Assess for Plasmodium parasites.
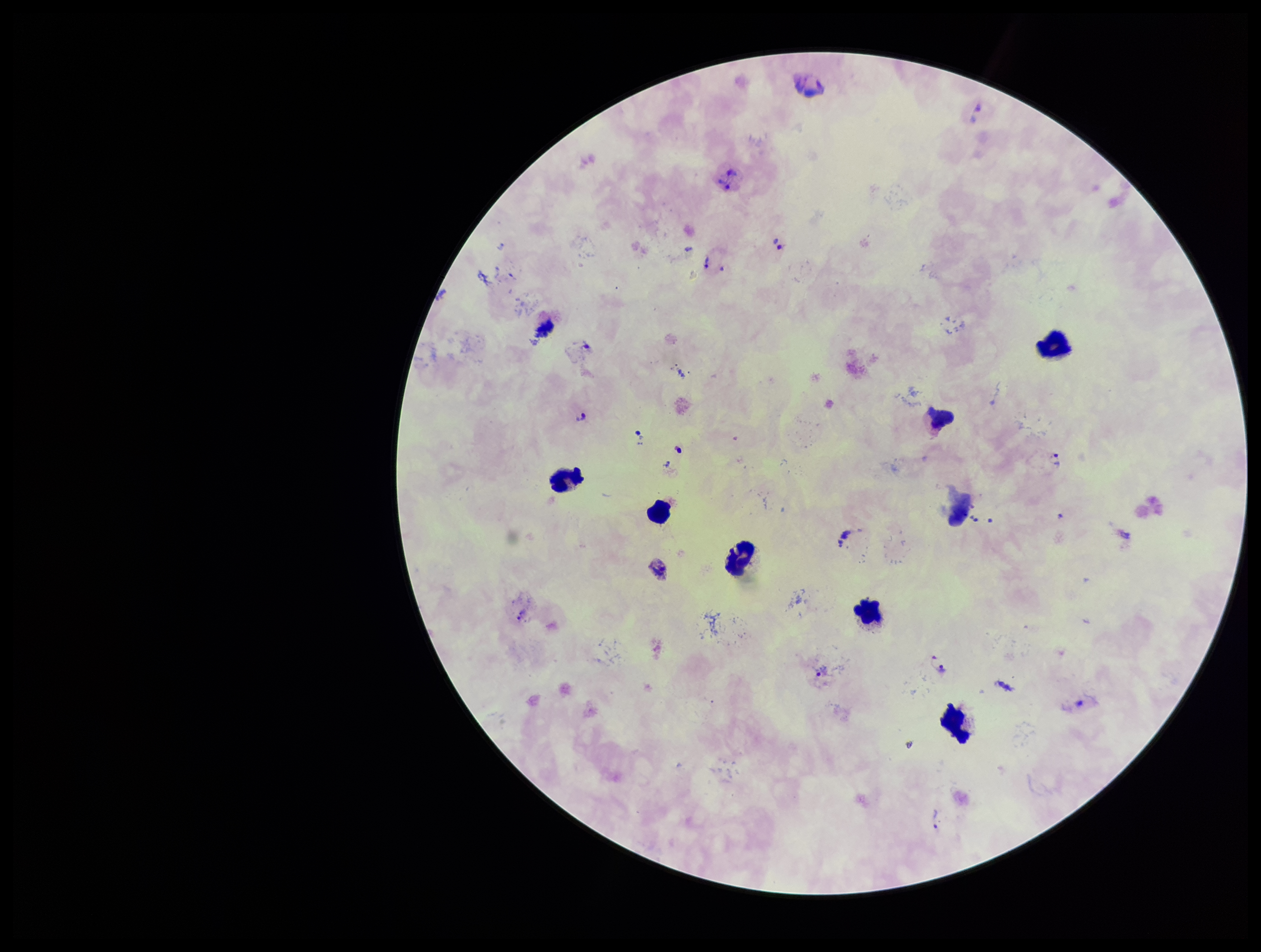
Identified.

Preparation: thick. Species reported for this patient: Plasmodium vivax. Parasite count: 20. Leukocyte count: 9. Image is 1261×952 pixels. Patient malaria status: positive. Photographed through the microscope eyepiece with a smartphone camera. Giemsa stain. Single field of view.